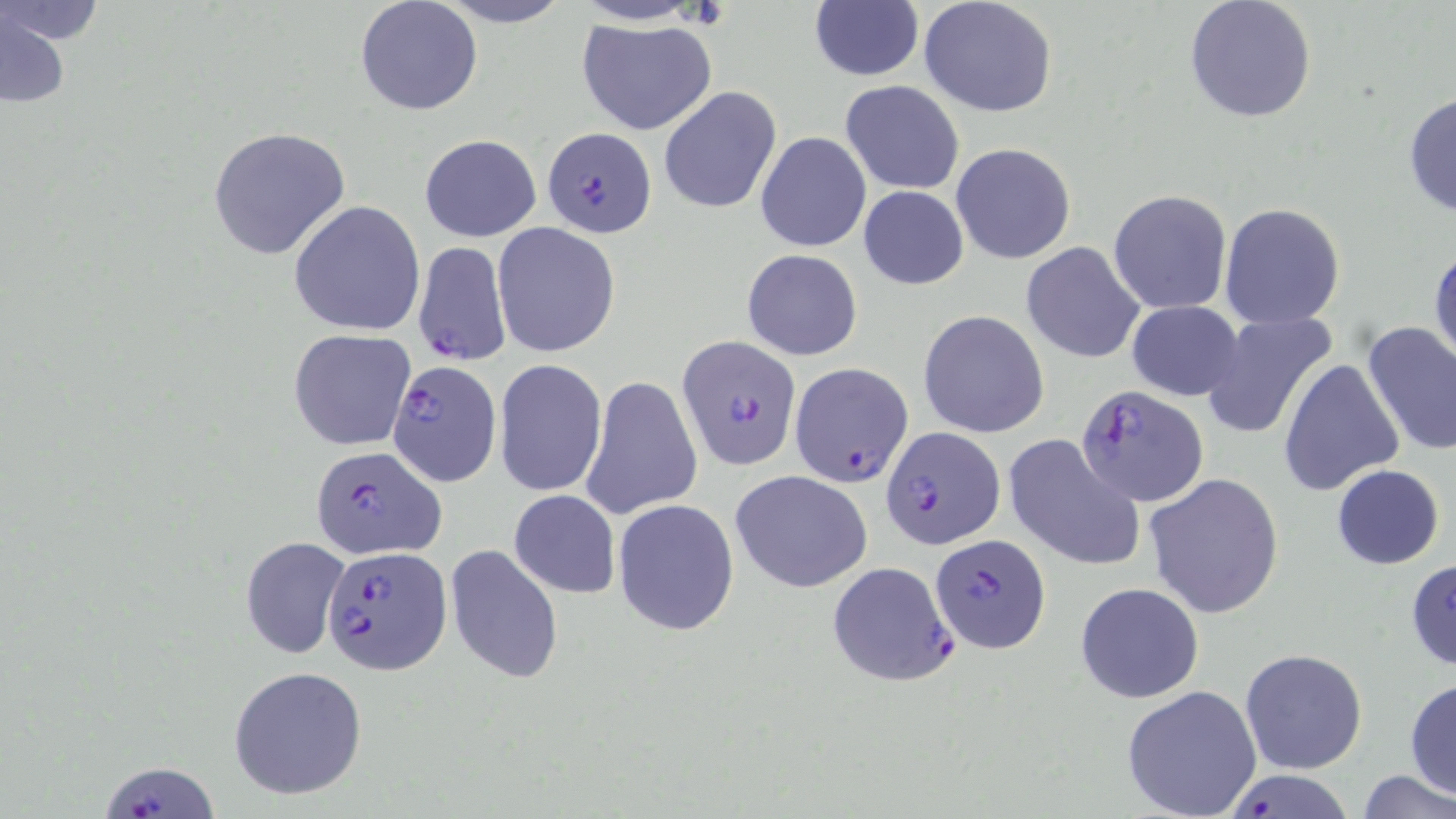

Plasmodium falciparum-infected red blood cell locations = approximate bounding boxes as named x1/y1/x2/y2 corners in pixels: (x1=542, y1=128, x2=657, y2=236), (x1=413, y1=241, x2=510, y2=366), (x1=675, y1=334, x2=799, y2=467), (x1=386, y1=361, x2=502, y2=487), (x1=790, y1=361, x2=914, y2=487), (x1=1076, y1=385, x2=1207, y2=506), (x1=882, y1=429, x2=1003, y2=550), (x1=309, y1=447, x2=447, y2=562), (x1=932, y1=534, x2=1051, y2=652), (x1=321, y1=545, x2=450, y2=674), (x1=827, y1=561, x2=959, y2=686), (x1=100, y1=757, x2=215, y2=817)
slide-level diagnosis = Plasmodium falciparum
modality = optical microscopy
preparation = thin blood smear
uninfected red blood cell locations = approximate bounding boxes as named x1/y1/x2/y2 corners in pixels: (x1=0, y1=0, x2=108, y2=48), (x1=356, y1=0, x2=483, y2=118), (x1=432, y1=0, x2=576, y2=28), (x1=918, y1=1, x2=1057, y2=118), (x1=1182, y1=1, x2=1316, y2=124), (x1=810, y1=3, x2=923, y2=81), (x1=1, y1=7, x2=73, y2=111), (x1=577, y1=17, x2=718, y2=135), (x1=840, y1=80, x2=965, y2=196), (x1=658, y1=86, x2=781, y2=213), (x1=1403, y1=91, x2=1456, y2=221), (x1=208, y1=126, x2=351, y2=260), (x1=755, y1=130, x2=871, y2=252), (x1=419, y1=133, x2=542, y2=241), (x1=950, y1=141, x2=1077, y2=265), (x1=859, y1=186, x2=969, y2=290), (x1=1108, y1=189, x2=1232, y2=314), (x1=288, y1=200, x2=426, y2=337), (x1=1219, y1=201, x2=1346, y2=329), (x1=492, y1=222, x2=620, y2=357), (x1=1429, y1=239, x2=1455, y2=371), (x1=1021, y1=241, x2=1145, y2=363), (x1=742, y1=248, x2=863, y2=361), (x1=1125, y1=299, x2=1246, y2=401), (x1=918, y1=308, x2=1049, y2=438), (x1=1200, y1=311, x2=1340, y2=440), (x1=1360, y1=321, x2=1456, y2=457), (x1=1235, y1=322, x2=1393, y2=465), (x1=288, y1=330, x2=417, y2=449), (x1=495, y1=358, x2=607, y2=498), (x1=1279, y1=359, x2=1405, y2=497), (x1=581, y1=374, x2=703, y2=520), (x1=1004, y1=434, x2=1146, y2=570), (x1=1331, y1=464, x2=1446, y2=570), (x1=730, y1=469, x2=873, y2=594), (x1=1143, y1=472, x2=1283, y2=618), (x1=509, y1=489, x2=620, y2=598), (x1=613, y1=499, x2=740, y2=635), (x1=240, y1=536, x2=349, y2=660), (x1=445, y1=544, x2=563, y2=686), (x1=1406, y1=557, x2=1456, y2=671), (x1=1073, y1=581, x2=1204, y2=704), (x1=1239, y1=647, x2=1368, y2=775), (x1=227, y1=665, x2=368, y2=800), (x1=1405, y1=677, x2=1456, y2=802), (x1=1120, y1=685, x2=1260, y2=819), (x1=1355, y1=770, x2=1456, y2=819), (x1=1224, y1=771, x2=1357, y2=817)
field of view = single
magnification = 1000x
image size = 1456×819 pixels
stain = May-Grünwald-Giemsa